Identify the blood parasite species.
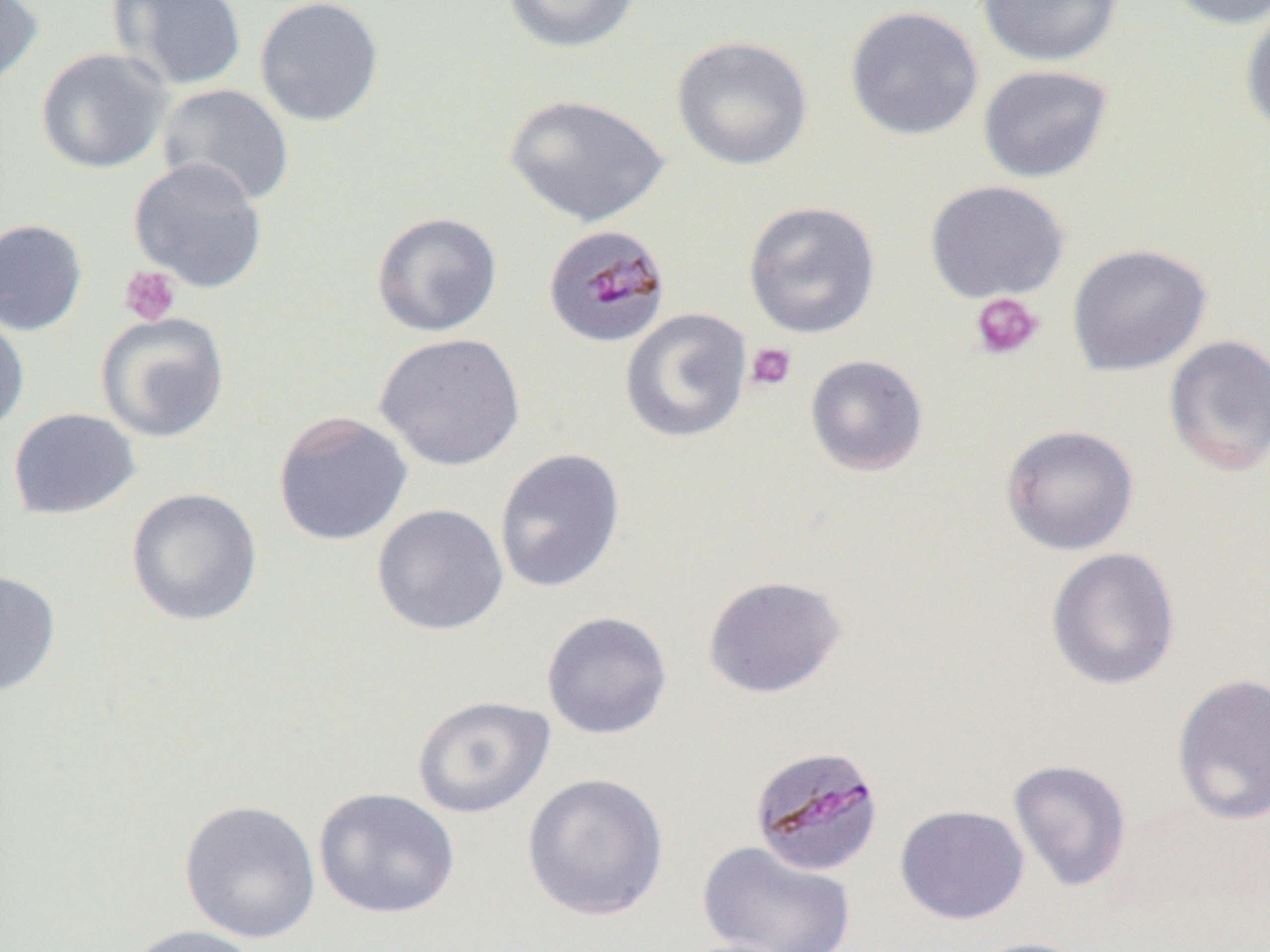

Plasmodium malariae.

magnification: 1000x
modality: light microscopy
uninfected_red_blood_cell_locations: 'approximate bounding boxes as (x1, y1, x2, y2) in pixels: (0, 0, 44, 89), (108, 0, 247, 91), (254, 0, 385, 127), (501, 0, 641, 53), (976, 0, 1125, 67), (1162, 0, 1270, 30), (845, 5, 984, 141), (1239, 5, 1270, 136), (671, 36, 813, 171), (35, 47, 173, 174), (977, 64, 1114, 184), (156, 83, 294, 208), (504, 93, 669, 227), (128, 157, 268, 294), (923, 180, 1069, 303), (743, 200, 881, 339), (371, 211, 502, 337), (0, 219, 88, 336), (1066, 243, 1212, 377), (620, 308, 752, 444), (0, 311, 30, 437), (95, 312, 230, 443), (374, 332, 526, 471), (1163, 335, 1270, 476), (805, 354, 929, 476), (7, 408, 140, 520), (273, 411, 413, 546), (1000, 424, 1139, 556), (494, 448, 626, 594), (126, 488, 263, 626), (372, 503, 509, 635), (1045, 547, 1180, 690), (0, 568, 61, 698), (702, 575, 846, 698), (541, 611, 673, 739), (1171, 673, 1270, 826), (413, 695, 555, 818), (1008, 759, 1132, 892), (522, 772, 669, 921), (313, 787, 460, 919), (178, 799, 321, 944), (894, 804, 1029, 925), (697, 840, 857, 952), (122, 924, 265, 952), (966, 937, 1096, 952), (667, 938, 803, 952)'
field_of_view: one of a larger specimen
preparation: thin blood smear
image_size: 1270×952 pixels
plasmodium_malariae_infected_red_blood_cell_locations: 'approximate bounding boxes as (x1, y1, x2, y2) in pixels: (543, 223, 670, 348), (748, 744, 885, 877)'
platelet_locations: 'approximate bounding boxes as (x1, y1, x2, y2) in pixels: (1, 217, 87, 334), (119, 265, 181, 326), (970, 292, 1044, 360), (745, 342, 797, 392)'